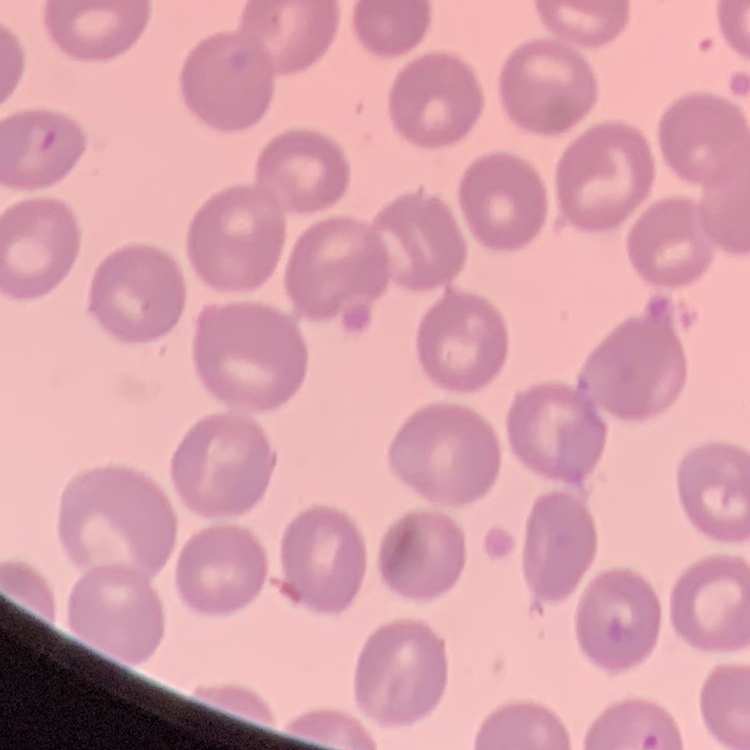
Summary:
  - Red blood cell morphology: no rouleaux formation
  - Preparation: thin blood film
  - Image type: square crop of a larger photomicrograph
  - Stain: Field's or Giemsa